Outline each Plasmodium falciparum-infected red blood cell.
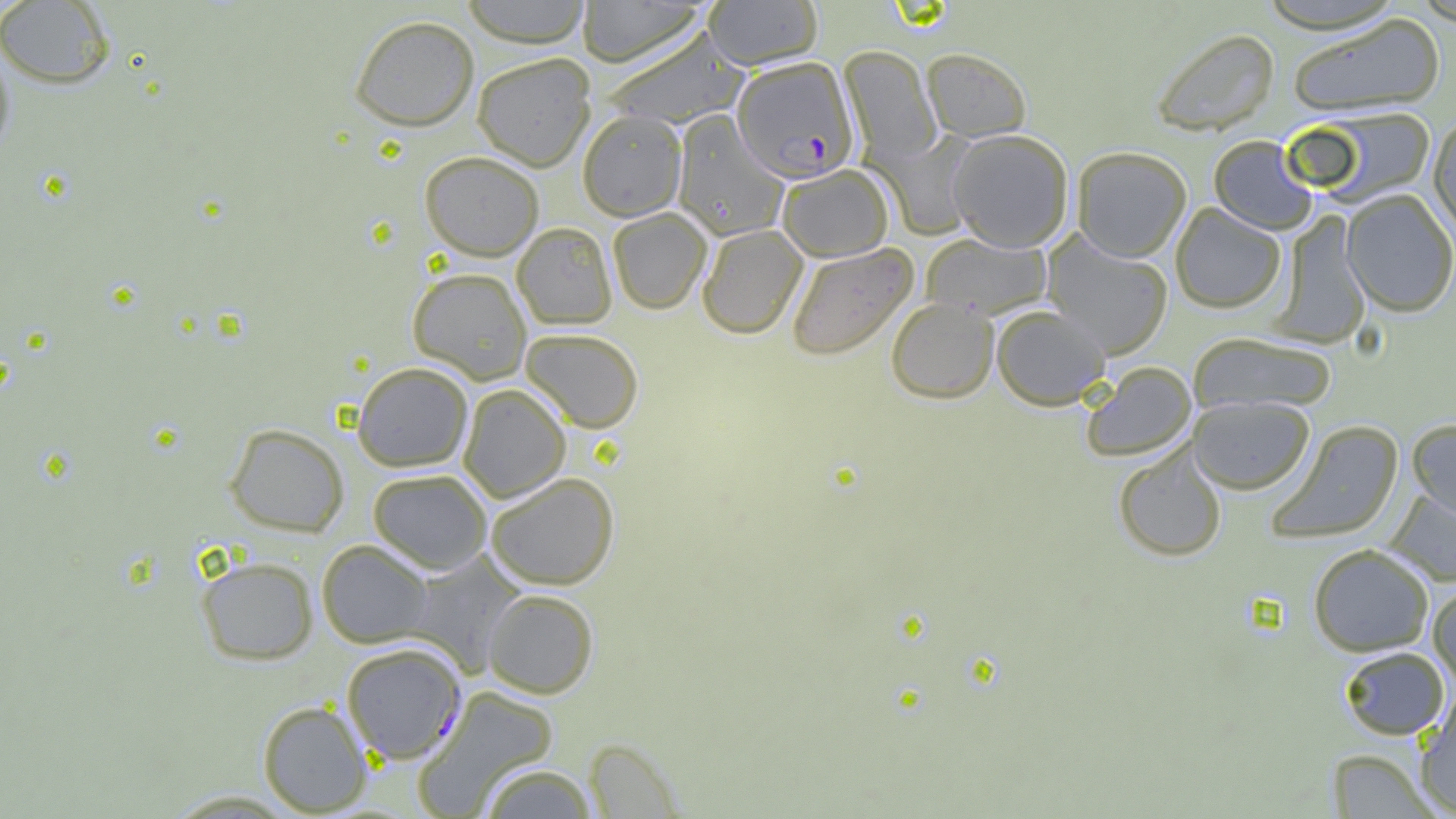

Approximate bounding boxes as (x1, y1, x2, y2) in pixels.
Plasmodium falciparum-infected red blood cells: (732, 56, 859, 183), (341, 642, 466, 764).

Summary:
  - Uninfected red blood cell locations: (459, 0, 593, 47), (576, 0, 709, 67), (703, 0, 823, 70), (1255, 0, 1407, 35), (0, 1, 116, 89), (1286, 14, 1445, 116), (349, 15, 479, 131), (602, 27, 750, 130), (1150, 28, 1279, 136), (0, 37, 16, 162), (838, 45, 942, 165), (921, 48, 1032, 142), (472, 53, 596, 171), (1296, 107, 1437, 207), (577, 110, 687, 221), (671, 112, 789, 242), (1428, 114, 1456, 239), (870, 130, 979, 240), (947, 130, 1074, 251), (1208, 135, 1318, 235), (1071, 146, 1191, 262), (420, 150, 544, 261), (776, 164, 894, 262), (1341, 189, 1456, 317), (1170, 203, 1286, 313), (607, 207, 712, 314), (1270, 211, 1371, 348), (512, 222, 617, 329), (697, 224, 807, 339), (921, 233, 1052, 319), (1041, 233, 1173, 360), (785, 243, 917, 361), (407, 266, 532, 383), (886, 297, 998, 403), (991, 305, 1110, 410), (520, 328, 644, 433), (1189, 333, 1337, 415), (352, 362, 473, 471), (1081, 362, 1197, 462), (457, 383, 571, 501), (1187, 396, 1315, 495), (1407, 419, 1456, 524), (1267, 420, 1405, 545), (225, 422, 348, 536), (1113, 443, 1227, 562), (367, 468, 492, 574), (485, 472, 619, 590), (1384, 489, 1456, 588), (316, 539, 433, 647), (1308, 543, 1434, 656), (406, 552, 526, 676), (197, 556, 318, 665), (1427, 584, 1456, 689), (483, 588, 599, 698), (1339, 646, 1449, 740), (411, 685, 560, 818), (1415, 692, 1456, 815), (258, 700, 372, 816), (583, 738, 683, 818), (1327, 748, 1439, 818), (478, 762, 599, 819), (159, 789, 304, 817)
  - Slide-level diagnosis: Plasmodium falciparum
  - Preparation: thin blood film
  - Modality: light microscopy
  - Image size: 1456×819 pixels
  - Field of view: single
  - Magnification: 1000x